Assess this cell for malaria.
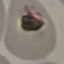

It is uninfected.

Summary:
  - Capture: smartphone through the microscope eyepiece
  - Preparation: thin blood smear
  - Stain: Giemsa
  - Image type: cell patch, automatically extracted from a larger field of view and resized to 64 × 64 pixels